Assess this cell for malaria.
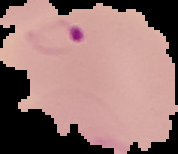
It is parasitized.

image type = segmented cell region with the area outside set to black
image size = 178×154 pixels
preparation = thin blood smear